State the blood parasite species.
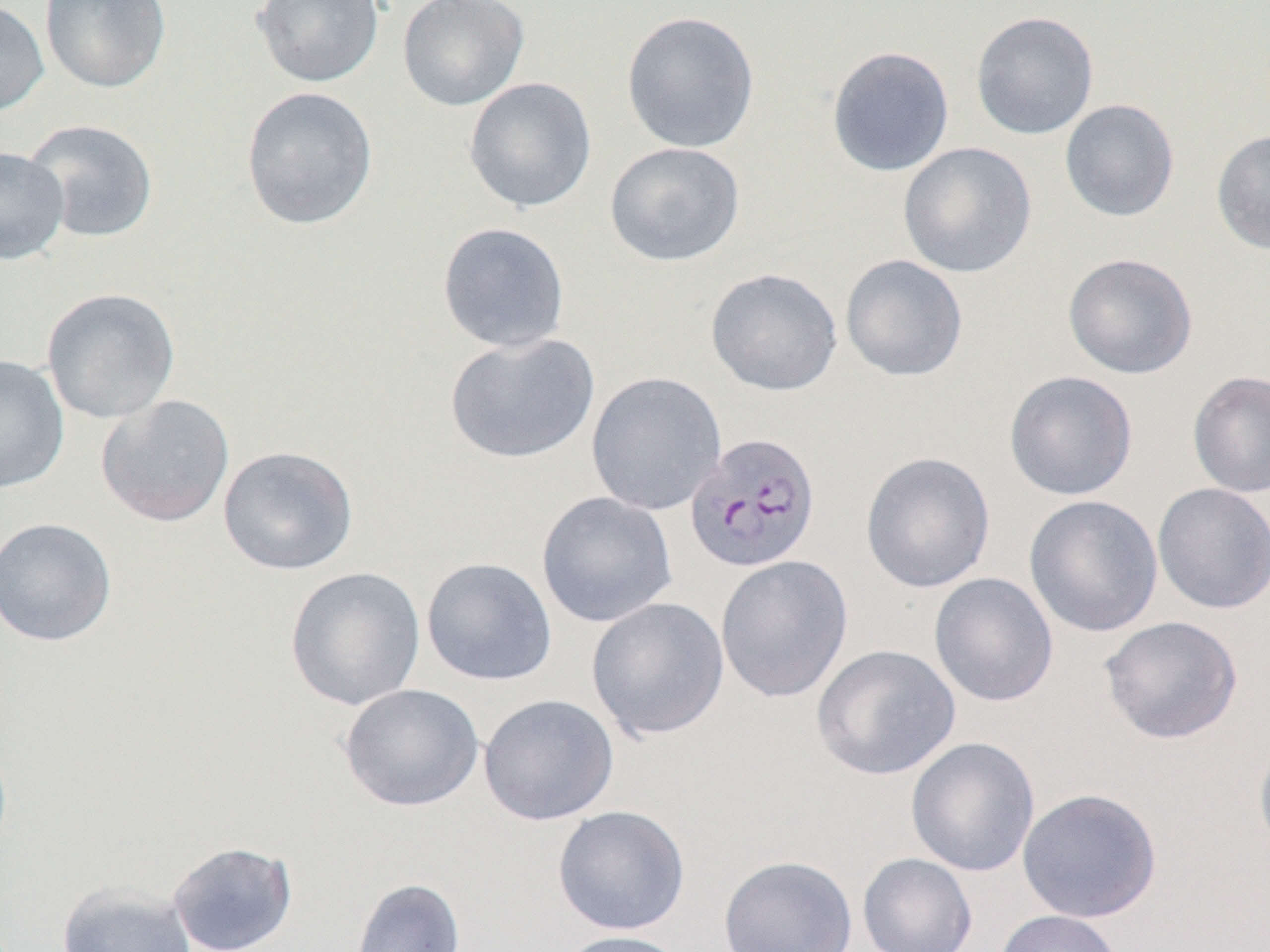

Plasmodium falciparum.

image_size: 1270×952 pixels
modality: optical microscopy
uninfected_red_blood_cell_locations: 'approximate bounding boxes as (x1,y1)-(x2,y2) corner pairs in pixels: (0,0)-(50,118), (40,0)-(172,94), (251,0)-(385,88), (397,0)-(530,112), (620,10)-(760,154), (970,11)-(1099,141), (826,46)-(955,177), (463,77)-(597,214), (240,85)-(379,231), (1059,98)-(1179,222), (21,118)-(159,243), (1211,128)-(1270,255), (604,141)-(745,267), (898,142)-(1037,279), (0,146)-(71,265), (437,221)-(571,353), (1063,252)-(1198,379), (839,254)-(968,381), (705,267)-(842,396), (41,287)-(181,424), (443,332)-(600,464), (0,355)-(70,494), (1003,370)-(1139,500), (1187,370)-(1270,498), (585,371)-(727,516), (95,393)-(236,528), (218,445)-(359,575), (860,451)-(996,594), (1152,483)-(1270,614), (536,491)-(678,628), (1023,494)-(1163,638), (0,516)-(118,647), (715,555)-(854,703), (421,556)-(557,686), (284,566)-(426,711), (929,572)-(1059,707), (585,596)-(730,742), (1099,615)-(1244,745), (810,644)-(960,780), (339,683)-(484,812), (478,693)-(619,826), (1253,734)-(1270,866), (906,736)-(1040,877), (1017,787)-(1162,923), (552,804)-(690,935), (167,841)-(297,952), (857,852)-(978,952), (718,855)-(858,952), (350,877)-(466,952), (56,880)-(197,952), (992,909)-(1124,952), (554,929)-(692,952)'
field_of_view: one of a larger specimen
plasmodium_falciparum_infected_red_blood_cell_locations: 'approximate bounding boxes as (x1,y1)-(x2,y2) corner pairs in pixels: (684,432)-(821,574)'
magnification: 1000x
preparation: thin blood film